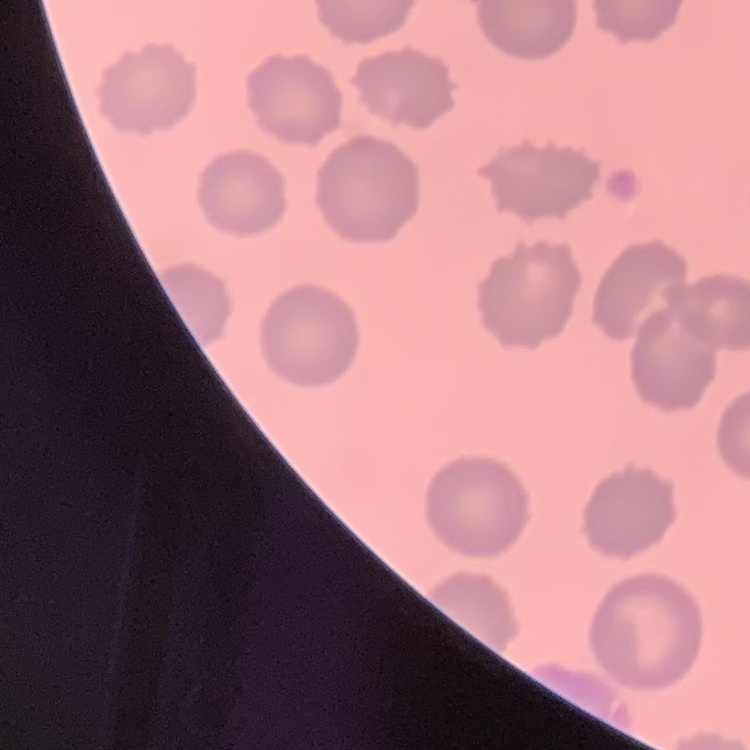

erythrocyte_morphology: no rouleaux formation
preparation: thin peripheral smear
image_type: one tile cut from a larger photomicrograph
stain: Field's or Giemsa